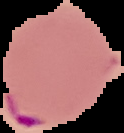

Summary:
  - Image size: 124×133 pixels
  - Image type: cell region segmented out of the field of view; surrounding area masked to black
  - Malaria status: parasitized
  - Preparation: thin blood smear